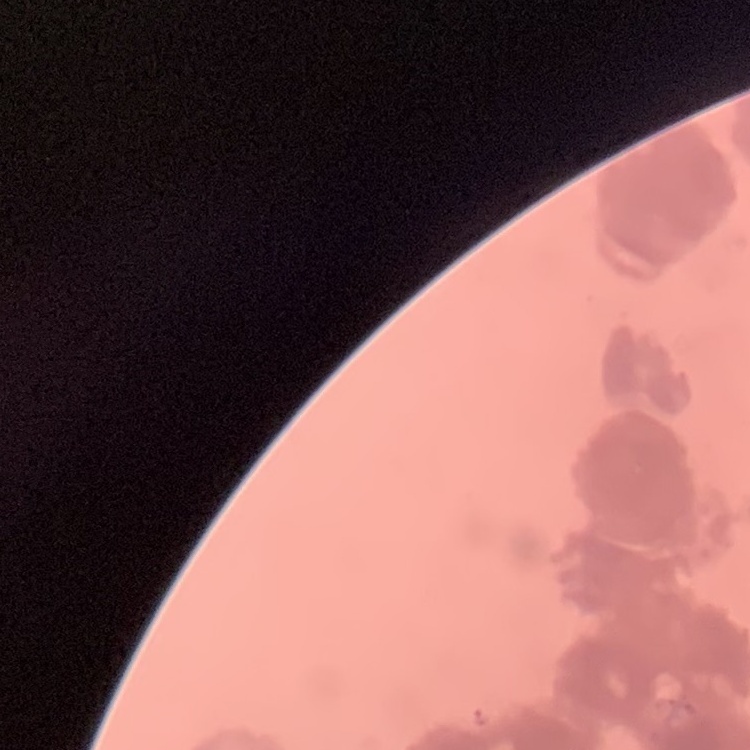 The red blood cells show rouleaux formation. Square crop of a larger photomicrograph. Field's or Giemsa stain. Thin blood film.